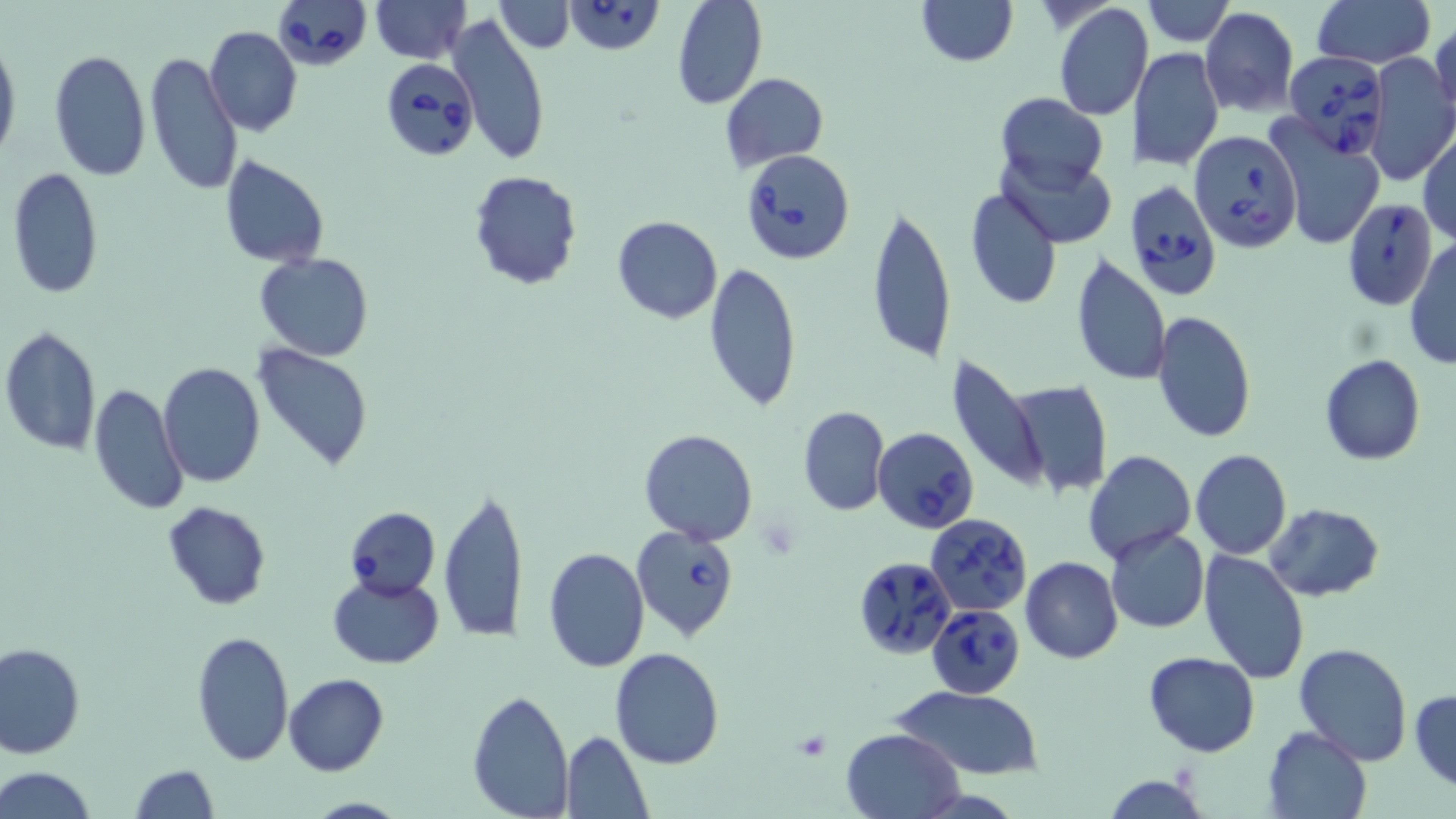
{
  "slide_level_diagnosis": "Babesia divergens",
  "stain": "May-Grünwald-Giemsa",
  "image_size": "1456×819 pixels",
  "uninfected_red_blood_cell_locations": "approximate bounding boxes as [x1, y1, x2, y2] in pixels: [372, 0, 469, 63], [494, 0, 574, 52], [671, 0, 768, 110], [915, 0, 1017, 66], [1143, 0, 1233, 46], [1313, 0, 1435, 71], [1052, 3, 1150, 119], [1200, 7, 1299, 117], [447, 14, 552, 166], [1428, 20, 1455, 122], [205, 26, 301, 136], [0, 37, 20, 167], [1131, 46, 1224, 172], [48, 49, 150, 180], [145, 50, 240, 197], [1366, 51, 1455, 187], [721, 72, 829, 172], [996, 92, 1109, 194], [1270, 121, 1387, 251], [1418, 129, 1456, 248], [219, 154, 330, 269], [7, 167, 104, 300], [468, 170, 583, 290], [963, 185, 1062, 311], [866, 203, 956, 367], [612, 215, 723, 324], [1405, 240, 1456, 368], [254, 251, 373, 362], [1070, 253, 1170, 389], [703, 260, 802, 412], [1153, 310, 1256, 443], [0, 325, 103, 456], [252, 341, 375, 471], [1320, 354, 1425, 466], [945, 355, 1045, 490], [158, 361, 265, 486], [1006, 378, 1113, 499], [88, 383, 188, 517], [797, 406, 890, 517], [639, 429, 759, 546], [1083, 450, 1195, 561], [1190, 450, 1292, 560], [438, 486, 527, 645], [162, 503, 271, 610], [1263, 503, 1385, 601], [1105, 526, 1210, 634], [542, 546, 649, 672], [1197, 550, 1310, 685], [1020, 556, 1123, 664], [327, 573, 445, 669], [191, 628, 294, 765], [0, 641, 85, 759], [1294, 643, 1413, 766], [610, 647, 725, 769], [1143, 652, 1260, 757], [284, 673, 388, 776], [891, 685, 1044, 780], [467, 686, 574, 816], [1410, 688, 1456, 791], [1262, 726, 1372, 819], [841, 728, 965, 819], [560, 730, 651, 816], [131, 763, 218, 819], [2, 767, 98, 819], [1102, 774, 1210, 818]",
  "magnification": "1000x",
  "babesia_divergens_infected_red_blood_cell_locations": "approximate bounding boxes as [x1, y1, x2, y2] in pixels: [273, 0, 370, 73], [564, 1, 667, 56], [1282, 51, 1390, 154], [378, 55, 477, 163], [1189, 129, 1303, 252], [739, 148, 856, 264], [1124, 180, 1221, 305], [1341, 198, 1439, 311], [876, 425, 978, 533], [342, 507, 442, 598], [924, 513, 1032, 614], [630, 523, 740, 643], [853, 553, 957, 660], [926, 603, 1025, 698]",
  "field_of_view": "single",
  "modality": "light microscopy",
  "preparation": "thin blood smear"
}